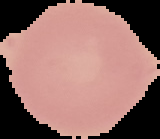

malaria status = uninfected
preparation = thin blood smear
image size = 160×139 pixels
image type = segmented cell region on a black background